Point out each malaria parasite.
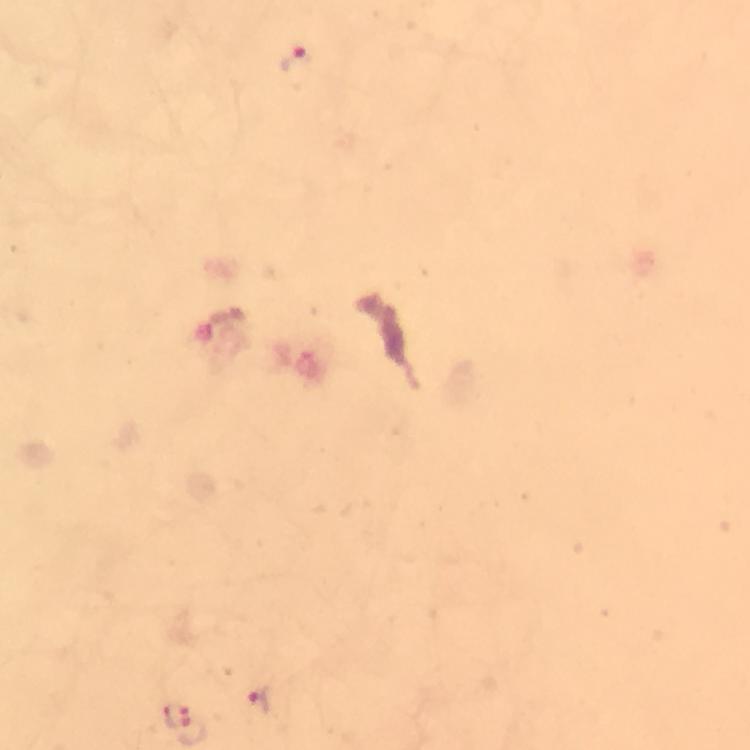
Approximate centers as [x, y] in pixels.
Malaria parasites: [295, 67], [255, 704], [177, 715].

image size = 750×750 pixels
context = from a diagnostic examination for malaria
magnification = 100x
preparation = thick blood smear
stain = Giemsa
capture = smartphone mounted on the microscope
immersion oil = used
cropped from = a single field of view